Identify the preparation type.
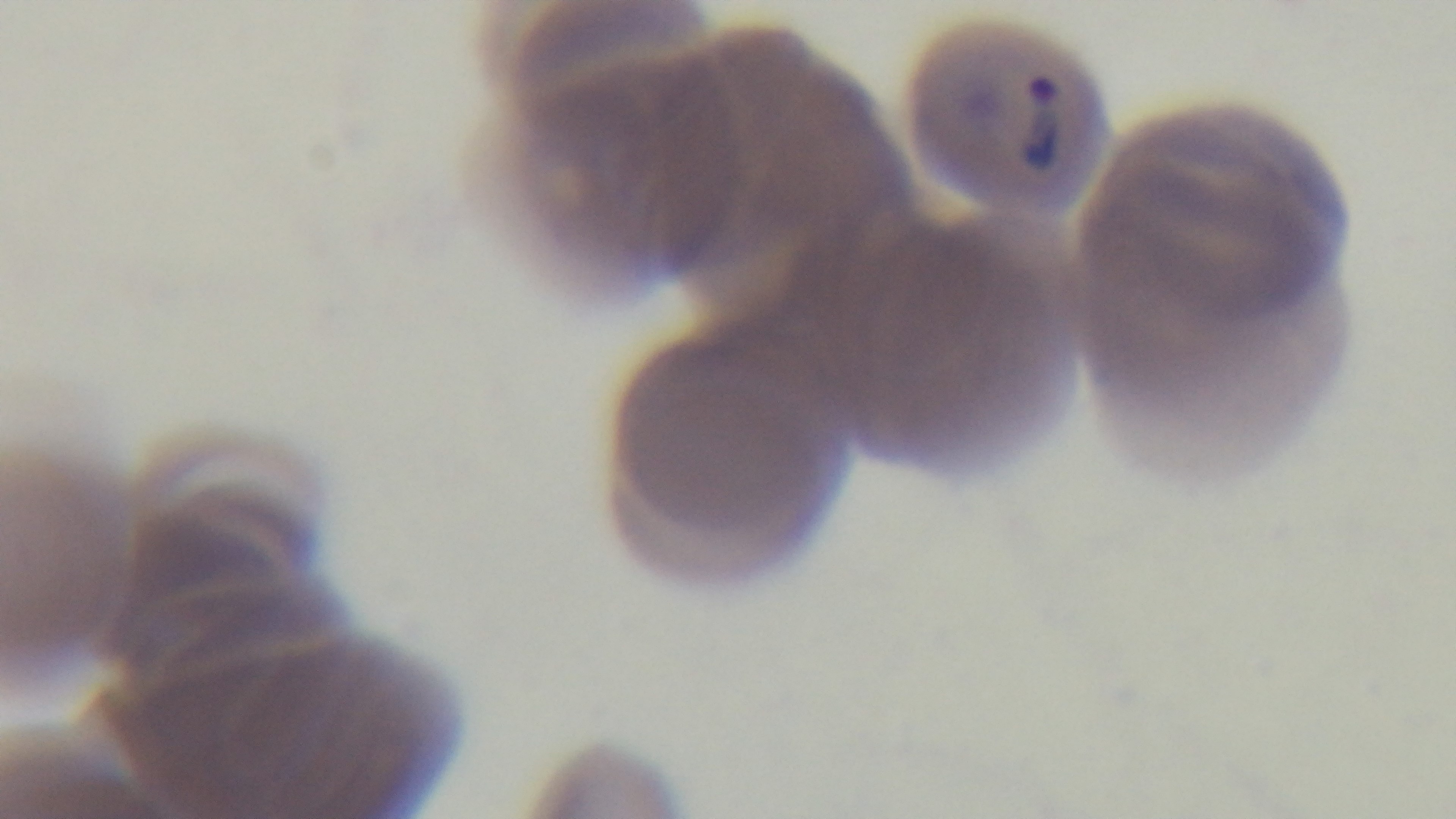
A thin smear.

{
  "objective": "100x oil immersion",
  "malaria_status": "positive",
  "modality": "light microscopy",
  "stain": "Giemsa",
  "capture": "mounted 4K digital camera",
  "field_of_view": "one from the slide"
}